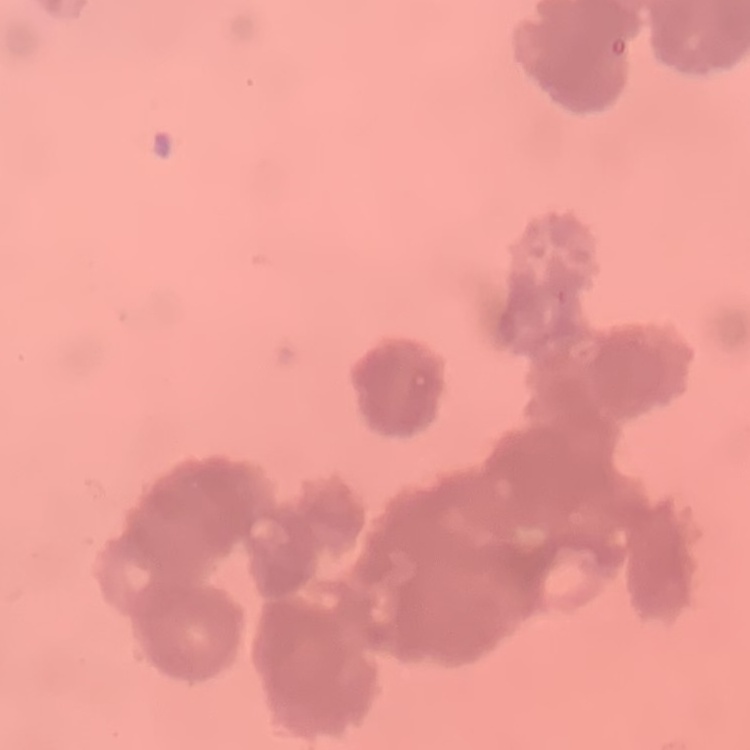
erythrocyte morphology = rouleaux formation
stain = Field's or Giemsa
preparation = thin blood film
image type = square crop of a larger photomicrograph